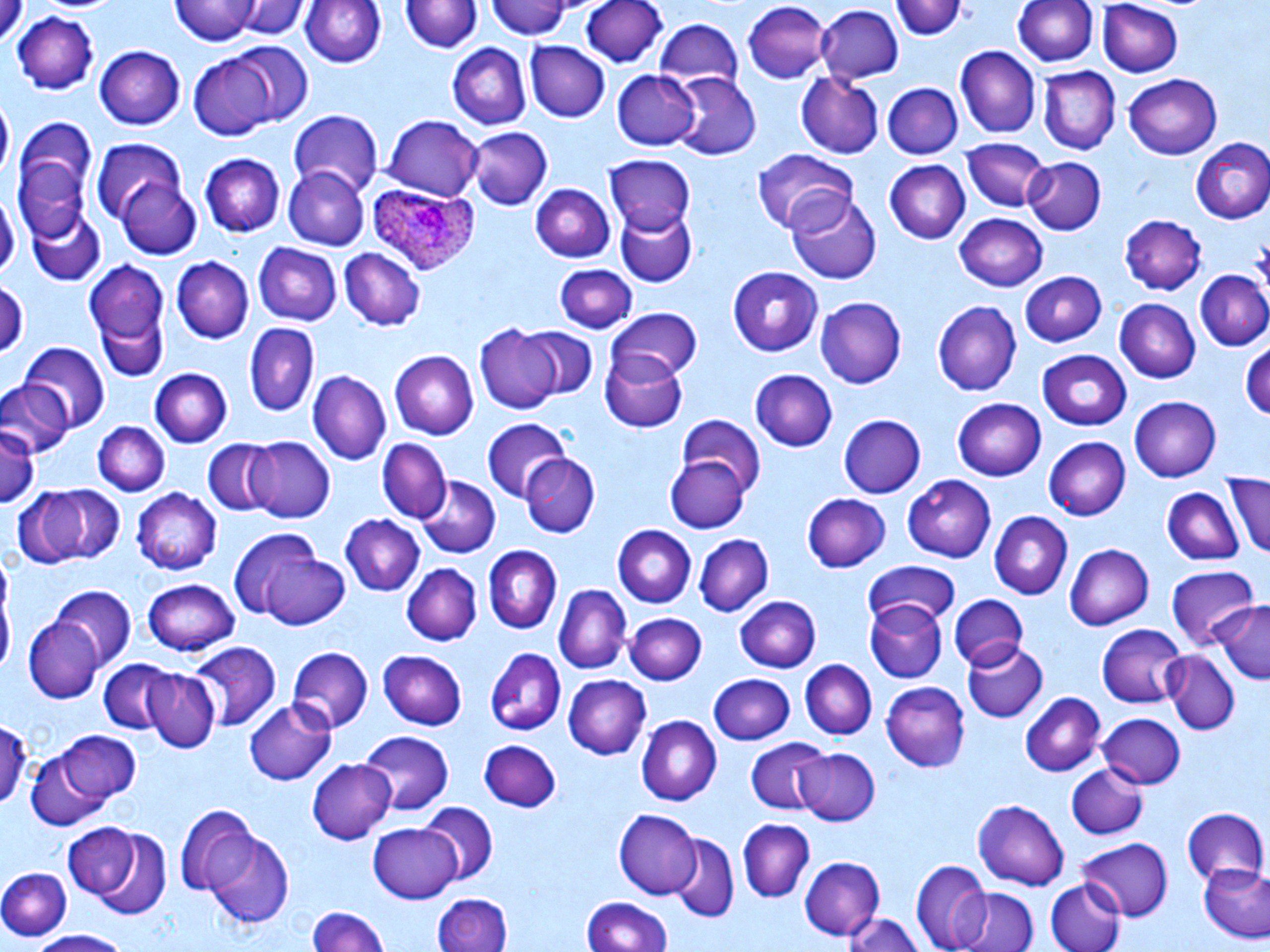

Summary:
  - Coordinate format: approximate bounding boxes as (x1, y1, x2, y2) in pixels
  - Plasmodium ovale-infected red blood cell locations: (368, 183, 479, 276)
  - Platelet locations: (1252, 235, 1270, 284)
  - Uninfected red blood cell locations: (171, 0, 264, 46), (230, 0, 304, 40), (300, 0, 385, 71), (488, 0, 576, 42), (579, 0, 670, 69), (895, 0, 965, 41), (1012, 0, 1097, 70), (401, 2, 480, 58), (1097, 2, 1182, 76), (741, 3, 833, 86), (815, 5, 905, 83), (13, 9, 102, 98), (652, 18, 744, 93), (526, 42, 609, 123), (209, 43, 315, 130), (446, 43, 529, 131), (95, 44, 185, 131), (955, 46, 1039, 137), (186, 56, 278, 141), (1041, 66, 1118, 153), (611, 69, 702, 151), (670, 71, 761, 161), (794, 71, 885, 158), (1120, 73, 1224, 161), (884, 82, 963, 160), (0, 102, 11, 180), (289, 111, 385, 198), (382, 115, 485, 199), (11, 119, 99, 239), (469, 128, 552, 210), (90, 137, 187, 228), (1190, 138, 1270, 224), (964, 140, 1047, 213), (752, 148, 857, 236), (605, 154, 697, 236), (201, 155, 286, 238), (1023, 159, 1104, 235), (883, 160, 971, 245), (282, 167, 368, 251), (116, 174, 204, 259), (531, 182, 617, 262), (783, 187, 880, 285), (1, 194, 18, 280), (26, 208, 106, 287), (615, 209, 696, 288), (954, 213, 1050, 292), (1120, 214, 1207, 294), (252, 242, 341, 326), (338, 247, 425, 331), (170, 256, 255, 343), (85, 258, 168, 354), (553, 264, 637, 333), (728, 265, 826, 354), (1018, 270, 1106, 346), (1193, 270, 1269, 352), (0, 280, 24, 361), (814, 296, 908, 389), (1115, 298, 1201, 385), (931, 300, 1022, 396), (93, 306, 168, 385), (609, 307, 704, 383), (243, 322, 319, 418), (473, 324, 562, 416), (516, 327, 600, 401), (19, 343, 110, 429), (1242, 344, 1270, 425), (599, 348, 688, 433), (1036, 350, 1133, 432), (390, 351, 479, 440), (148, 368, 230, 447), (750, 368, 838, 453), (308, 370, 390, 465), (0, 377, 72, 460), (1128, 394, 1221, 481), (953, 398, 1048, 480), (675, 414, 765, 495), (837, 414, 926, 500), (480, 417, 574, 501), (93, 419, 170, 495), (0, 420, 40, 513), (1044, 436, 1131, 518), (246, 437, 336, 523), (202, 440, 282, 517), (379, 440, 451, 523), (664, 453, 750, 533), (521, 454, 600, 540), (1226, 472, 1270, 561), (902, 473, 996, 562), (413, 475, 499, 559), (10, 484, 119, 573), (134, 487, 224, 575), (1161, 488, 1243, 568), (803, 491, 891, 574), (989, 511, 1072, 600), (339, 512, 425, 595), (615, 524, 696, 606), (240, 531, 348, 630), (693, 533, 773, 615), (1065, 544, 1153, 631), (482, 545, 560, 636), (863, 561, 960, 623), (402, 563, 481, 646), (1165, 563, 1260, 650), (142, 577, 241, 657), (0, 580, 13, 683), (553, 583, 631, 671), (52, 585, 136, 669), (947, 594, 1029, 670), (733, 595, 821, 672), (866, 599, 947, 684), (1213, 602, 1270, 683), (625, 611, 706, 685), (26, 616, 105, 704), (1095, 621, 1186, 710), (1107, 633, 1241, 719), (961, 639, 1048, 723), (188, 642, 278, 731), (288, 646, 372, 731), (377, 648, 467, 731), (487, 648, 567, 735), (1162, 653, 1239, 737), (97, 659, 175, 734), (800, 659, 876, 739), (143, 669, 220, 753), (707, 673, 796, 745), (562, 675, 652, 761), (880, 680, 971, 771), (1020, 694, 1105, 777), (243, 699, 339, 786), (1098, 712, 1184, 788), (636, 716, 721, 806), (0, 718, 30, 813), (53, 730, 140, 807), (359, 731, 454, 814), (478, 738, 563, 811), (744, 738, 831, 816), (23, 747, 121, 834), (791, 747, 879, 826), (308, 758, 397, 844), (1067, 764, 1147, 841), (971, 799, 1070, 891), (419, 802, 498, 885), (175, 806, 260, 898), (1181, 808, 1268, 889), (614, 810, 702, 900), (738, 820, 813, 901), (368, 821, 464, 904), (62, 822, 144, 906), (86, 829, 173, 918), (204, 834, 297, 929), (670, 836, 738, 920), (1078, 837, 1173, 922), (801, 856, 885, 941), (910, 859, 992, 950), (1197, 859, 1270, 944), (0, 867, 72, 940), (1044, 878, 1125, 952), (956, 886, 1038, 952), (434, 894, 511, 952), (582, 897, 672, 952), (306, 903, 387, 952), (842, 910, 926, 952), (25, 930, 128, 952)
  - Slide-level diagnosis: Plasmodium ovale
  - Stain: May-Grünwald-Giemsa
  - Field of view: single
  - Modality: light microscopy
  - Image size: 1270×952 pixels
  - Preparation: thin blood smear
  - Magnification: 1000x